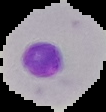

Summary:
  - Image type: segmented cell region on a black background
  - Image size: 106×112 pixels
  - Malaria status: parasitized
  - Preparation: thin blood smear